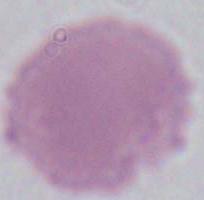
Summary:
  - Magnification: 1000x
  - Identification: red blood cell
  - Modality: micrograph